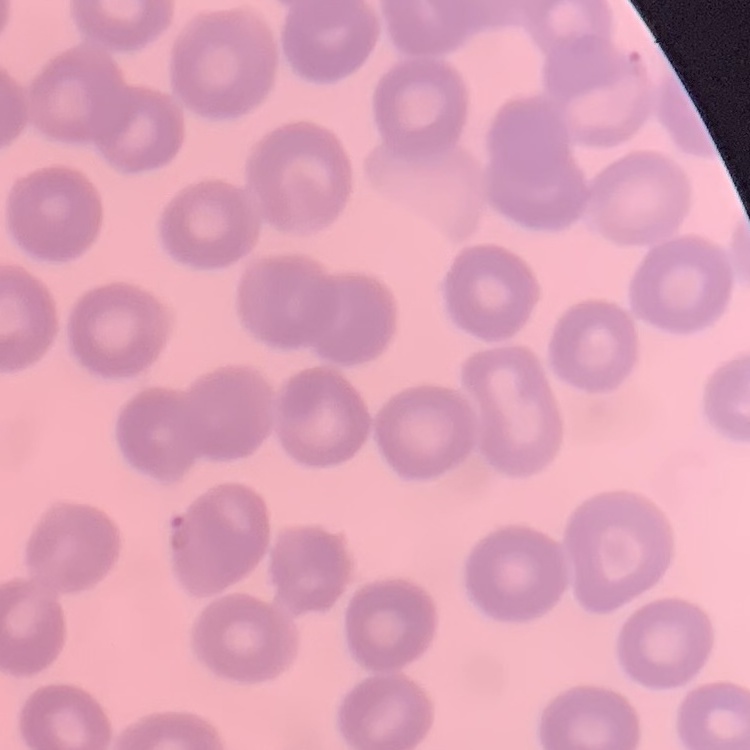
Summary:
  - Erythrocyte morphology: no rouleaux formation
  - Image type: one tile cut from a larger photomicrograph
  - Stain: Field's or Giemsa
  - Preparation: thin peripheral smear